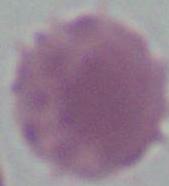
Summary:
  - Identification: red blood cell
  - Modality: micrograph
  - Magnification: 1000x